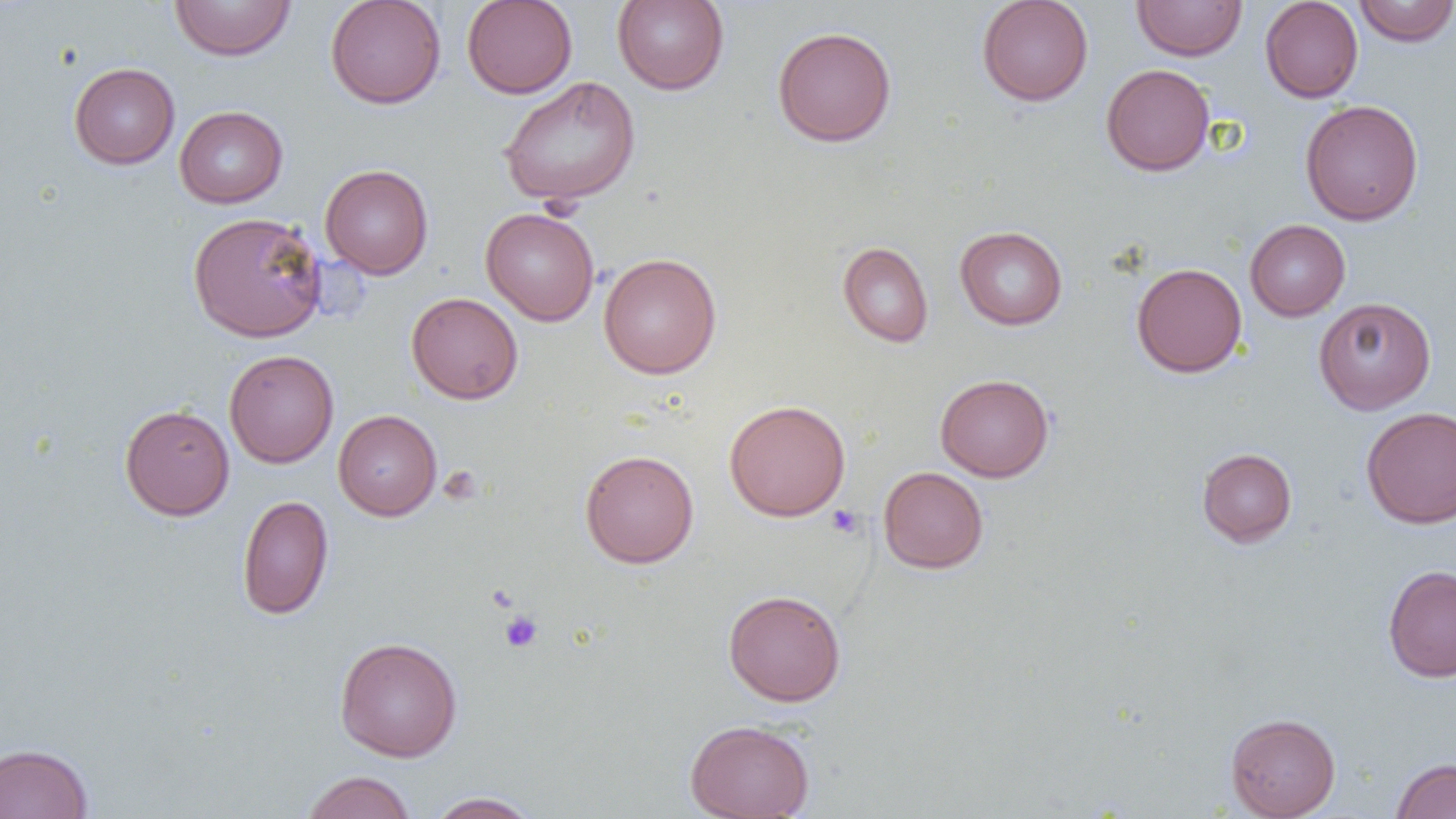
slide-level diagnosis = negative for blood parasites
uninfected red blood cell locations = approximate bounding boxes as (x1,y1)-(x2,y2) corner pairs in pixels: (169,0)-(296,61), (325,0)-(446,109), (461,0)-(578,99), (612,0)-(729,95), (976,0)-(1093,106), (1260,0)-(1363,103), (1353,0)-(1456,46), (1132,1)-(1247,60), (772,25)-(897,147), (68,62)-(180,169), (1101,63)-(1215,176), (498,75)-(641,207), (1300,99)-(1424,225), (174,105)-(288,208), (320,163)-(433,279), (480,207)-(600,326), (187,211)-(328,342), (1245,219)-(1350,321), (954,225)-(1068,330), (837,241)-(933,347), (598,252)-(722,379), (1131,262)-(1247,378), (406,291)-(523,404), (1313,297)-(1436,415), (224,349)-(339,468), (935,373)-(1054,482), (723,399)-(851,522), (119,404)-(235,520), (1360,406)-(1456,529), (333,409)-(442,521), (1196,448)-(1297,547), (580,449)-(699,568), (878,466)-(989,574), (237,495)-(333,620), (1383,564)-(1456,682), (722,589)-(847,706), (334,636)-(463,762), (1225,713)-(1340,819), (684,718)-(815,819), (0,743)-(93,819), (1391,757)-(1456,818), (301,770)-(417,819), (425,791)-(542,819)
modality = optical microscopy
field of view = single
image size = 1456×819 pixels
platelet locations = approximate bounding boxes as (x1,y1)-(x2,y2) corner pairs in pixels: (439,466)-(483,504), (826,505)-(864,538), (499,610)-(543,653)
magnification = 1000x
preparation = thin blood film